Identify the parasite.
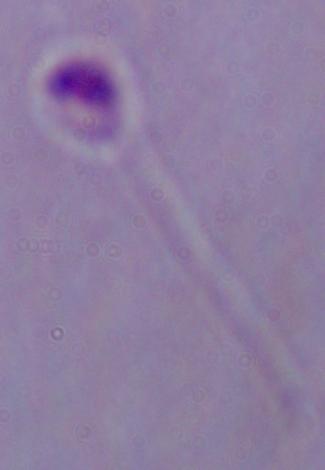

Leishmania.

Captured at 1000x magnification. Photomicrograph.